Assess this cell for malaria.
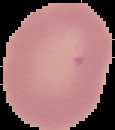

It is uninfected.

image type = cell region segmented out of the field of view; surrounding area masked to black
image size = 115×130 pixels
preparation = thin blood film